Identify the blood parasite species.
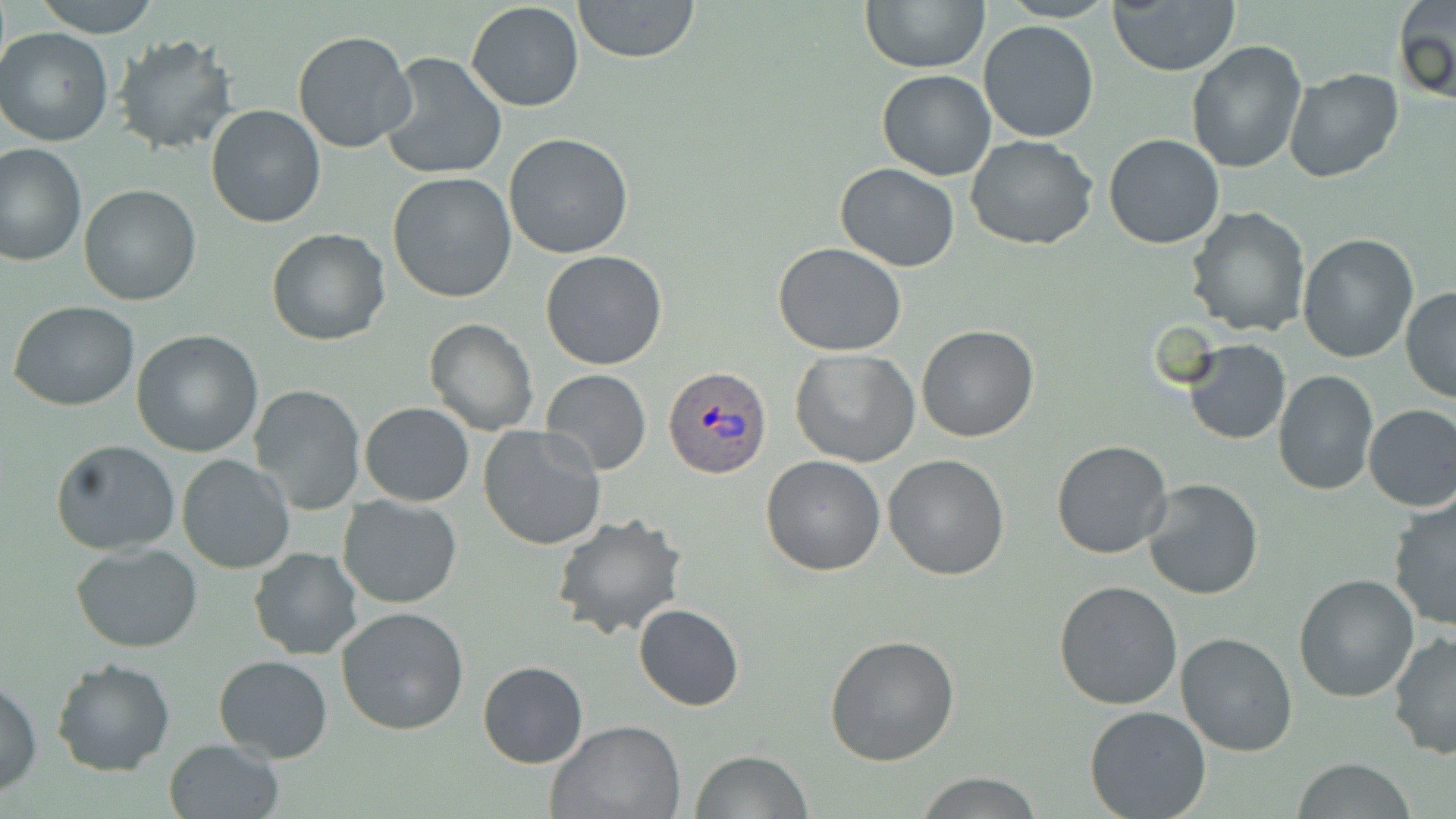
Plasmodium ovale.

Summary:
  - Coordinate format: approximate bounding boxes as (x1, y1, x2, y2) in pixels
  - Uninfected red blood cell locations: (34, 0, 159, 37), (571, 0, 702, 63), (861, 0, 988, 72), (1108, 1, 1240, 76), (1394, 1, 1455, 106), (465, 2, 585, 112), (978, 20, 1099, 143), (1, 27, 117, 146), (293, 30, 419, 155), (113, 33, 236, 154), (1185, 39, 1308, 175), (381, 52, 507, 181), (1283, 67, 1403, 183), (878, 68, 996, 180), (206, 104, 326, 228), (1104, 132, 1224, 249), (504, 133, 635, 259), (966, 135, 1098, 251), (0, 142, 86, 267), (834, 163, 960, 271), (387, 170, 517, 304), (79, 183, 202, 305), (1185, 205, 1310, 337), (266, 227, 391, 345), (1296, 232, 1420, 362), (773, 242, 907, 356), (540, 249, 669, 370), (1400, 287, 1456, 403), (8, 300, 140, 412), (424, 319, 538, 437), (916, 325, 1040, 443), (131, 329, 263, 457), (1185, 341, 1291, 445), (790, 348, 920, 467), (540, 368, 651, 476), (1272, 370, 1379, 496), (249, 384, 366, 513), (359, 402, 475, 507), (1362, 403, 1456, 512), (477, 424, 606, 551), (1051, 438, 1173, 559), (50, 439, 182, 553), (883, 453, 1011, 579), (175, 454, 297, 575), (760, 454, 887, 576), (1142, 477, 1263, 600), (336, 493, 463, 608), (1386, 496, 1456, 633), (552, 512, 687, 638), (71, 541, 203, 652), (248, 547, 363, 661), (1294, 573, 1419, 703), (1054, 579, 1184, 709), (335, 604, 470, 736), (633, 604, 743, 711), (1173, 633, 1299, 757), (1388, 633, 1456, 761), (824, 634, 960, 765), (213, 654, 332, 763), (50, 656, 176, 776), (477, 661, 587, 768), (1, 679, 44, 797), (1084, 706, 1212, 818), (543, 719, 685, 819), (162, 739, 287, 819), (689, 750, 813, 819), (1292, 758, 1417, 818), (912, 770, 1045, 818)
  - Plasmodium ovale-infected red blood cell locations: (663, 365, 769, 478)
  - Stain: May-Grünwald-Giemsa
  - Modality: optical microscopy
  - Field of view: one of a larger specimen
  - Magnification: 1000x
  - Preparation: thin blood smear
  - Image size: 1456×819 pixels